Report the malaria status of this cell.
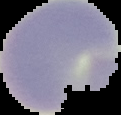

It is uninfected.

preparation = thin blood film
image size = 121×115 pixels
image type = cell region segmented out of the field of view; surrounding area masked to black